Outline platelets.
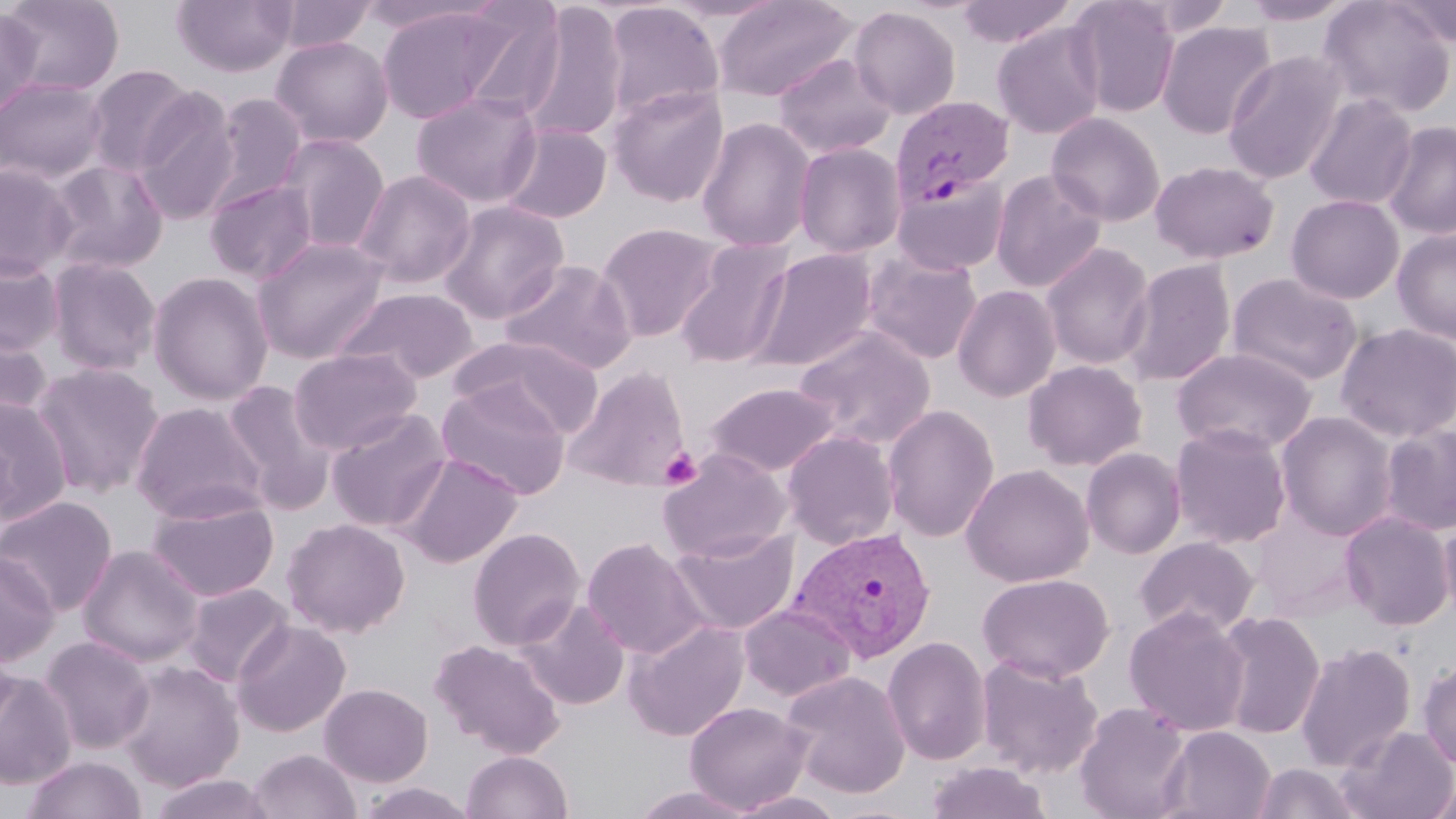
Approximate bounding boxes as (x1,y1)-(x2,y2) corner pairs in pixels.
Platelets: (659,447)-(701,490).

Summary:
  - Uninfected red blood cell locations: (1,0)-(125,96), (171,0)-(298,76), (272,0)-(378,52), (446,0)-(568,120), (712,0)-(856,102), (955,0)-(1077,48), (1067,0)-(1182,117), (1317,0)-(1456,118), (1241,1)-(1357,26), (519,2)-(628,143), (601,2)-(725,124), (1387,2)-(1456,47), (376,5)-(522,124), (0,6)-(43,119), (848,6)-(962,119), (991,20)-(1107,140), (1156,20)-(1277,139), (270,35)-(393,148), (1223,50)-(1347,184), (773,52)-(897,159), (83,64)-(198,178), (0,77)-(109,184), (607,86)-(729,208), (132,89)-(240,225), (410,91)-(542,208), (208,92)-(307,208), (1303,93)-(1418,211), (1046,112)-(1166,226), (696,117)-(816,252), (1382,121)-(1456,240), (498,123)-(612,225), (275,133)-(390,253), (793,142)-(906,258), (42,159)-(170,275), (1149,160)-(1280,265), (0,163)-(77,278), (990,168)-(1107,294), (352,169)-(476,289), (893,176)-(1009,275), (204,178)-(318,285), (1286,194)-(1405,304), (438,200)-(569,323), (596,222)-(724,342), (1392,228)-(1456,343), (251,236)-(389,363), (673,239)-(794,369), (1041,242)-(1156,370), (747,249)-(878,372), (861,250)-(983,364), (0,255)-(64,355), (46,257)-(161,376), (1121,258)-(1237,386), (499,259)-(637,375), (148,271)-(274,405), (1226,272)-(1362,386), (952,283)-(1061,401), (332,286)-(479,384), (1336,323)-(1456,443), (0,324)-(53,424), (794,326)-(936,447), (450,337)-(604,437), (1171,347)-(1317,455), (288,348)-(421,454), (1023,359)-(1147,471), (31,363)-(164,497), (565,366)-(691,490), (221,380)-(335,509), (435,382)-(571,500), (706,382)-(840,476), (0,396)-(73,522), (131,401)-(266,521), (882,405)-(1000,542), (326,407)-(452,533), (1276,411)-(1397,540), (1169,422)-(1293,548), (1380,424)-(1456,536), (781,429)-(900,550), (1081,446)-(1186,559), (657,449)-(792,562), (397,453)-(521,568), (961,463)-(1095,587), (147,492)-(279,602), (0,496)-(117,616), (1340,510)-(1454,630), (1251,511)-(1366,620), (1439,516)-(1456,623), (282,518)-(410,637), (467,527)-(585,650), (671,528)-(799,634), (1133,536)-(1259,638), (582,537)-(710,660), (77,544)-(204,666), (0,551)-(59,666), (976,572)-(1114,682), (182,583)-(294,686), (516,598)-(631,710), (739,603)-(856,702), (1123,606)-(1251,736), (1215,609)-(1326,739), (231,619)-(351,737), (624,619)-(750,741), (40,636)-(155,753), (881,636)-(992,765), (0,637)-(19,744), (429,638)-(566,758), (1295,641)-(1416,771), (976,654)-(1103,778), (1417,658)-(1456,771), (115,660)-(245,791), (0,669)-(77,789), (781,670)-(912,799), (319,682)-(433,786), (685,701)-(812,813), (1074,701)-(1193,819), (1159,725)-(1276,819), (1337,725)-(1456,819), (248,748)-(361,819), (461,750)-(573,818), (20,755)-(146,819), (923,760)-(1054,819), (1251,762)-(1363,819), (149,773)-(275,819), (1426,774)-(1456,819), (355,782)-(479,819), (629,786)-(758,819), (727,791)-(848,819)
  - Plasmodium vivax-infected red blood cell locations: (890,95)-(1014,210), (789,526)-(937,663)
  - Slide-level diagnosis: Plasmodium vivax
  - Image size: 1456×819 pixels
  - Stain: May-Grünwald-Giemsa
  - Magnification: 1000x
  - Field of view: single
  - Modality: optical microscopy
  - Preparation: thin blood smear